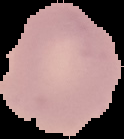

result = no Plasmodium parasites seen
image type = segmented cell region on a black background
image size = 124×139 pixels
preparation = thin blood smear